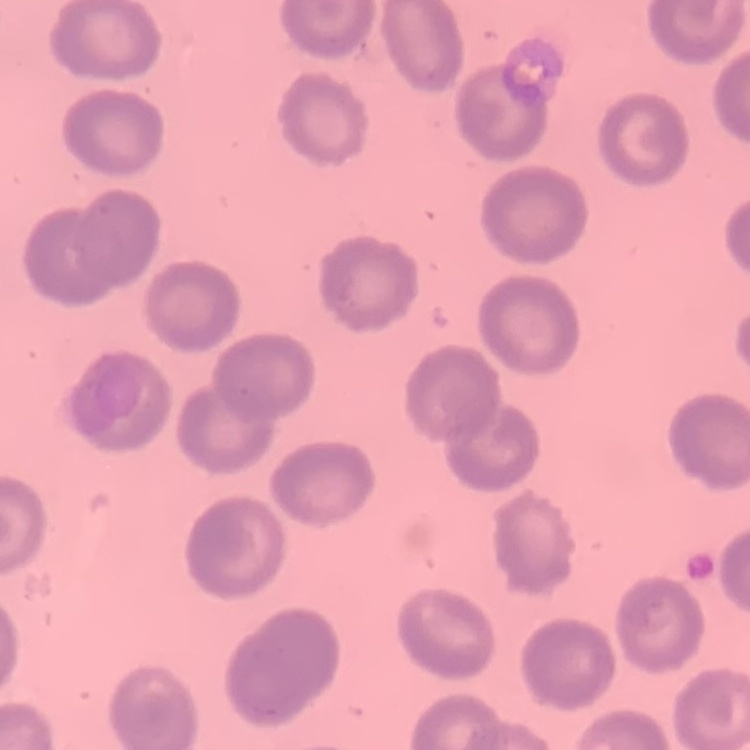

Summary:
  - Erythrocyte morphology: no rouleaux formation
  - Stain: Field's or Giemsa
  - Preparation: thin blood film
  - Image type: one tile cut from a larger photomicrograph